Classify this cell by malaria status.
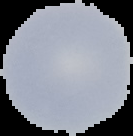
It is uninfected.

Cell region segmented out of the field of view; the surrounding area is masked to black. Image is 133×136 pixels. From a thin blood smear.